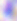

Summary:
  - Identification: Toxoplasma gondii
  - Modality: micrograph
  - Magnification: 400x